Identify the parasite.
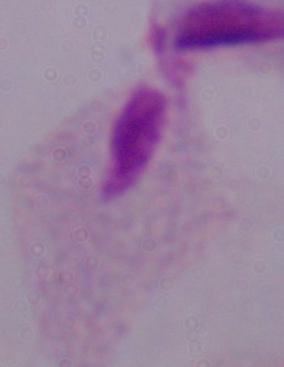
A trichomonad.

magnification: 1000x
modality: micrograph